Classify this cell by malaria status.
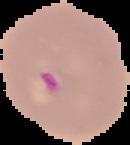

Parasitized.

Summary:
  - Image type: segmented cell region on a black background
  - Image size: 130×145 pixels
  - Preparation: thin blood film